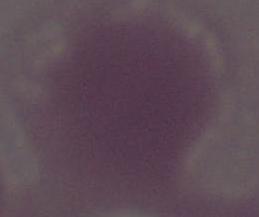

1000x magnification. A red blood cell is shown. Micrograph.